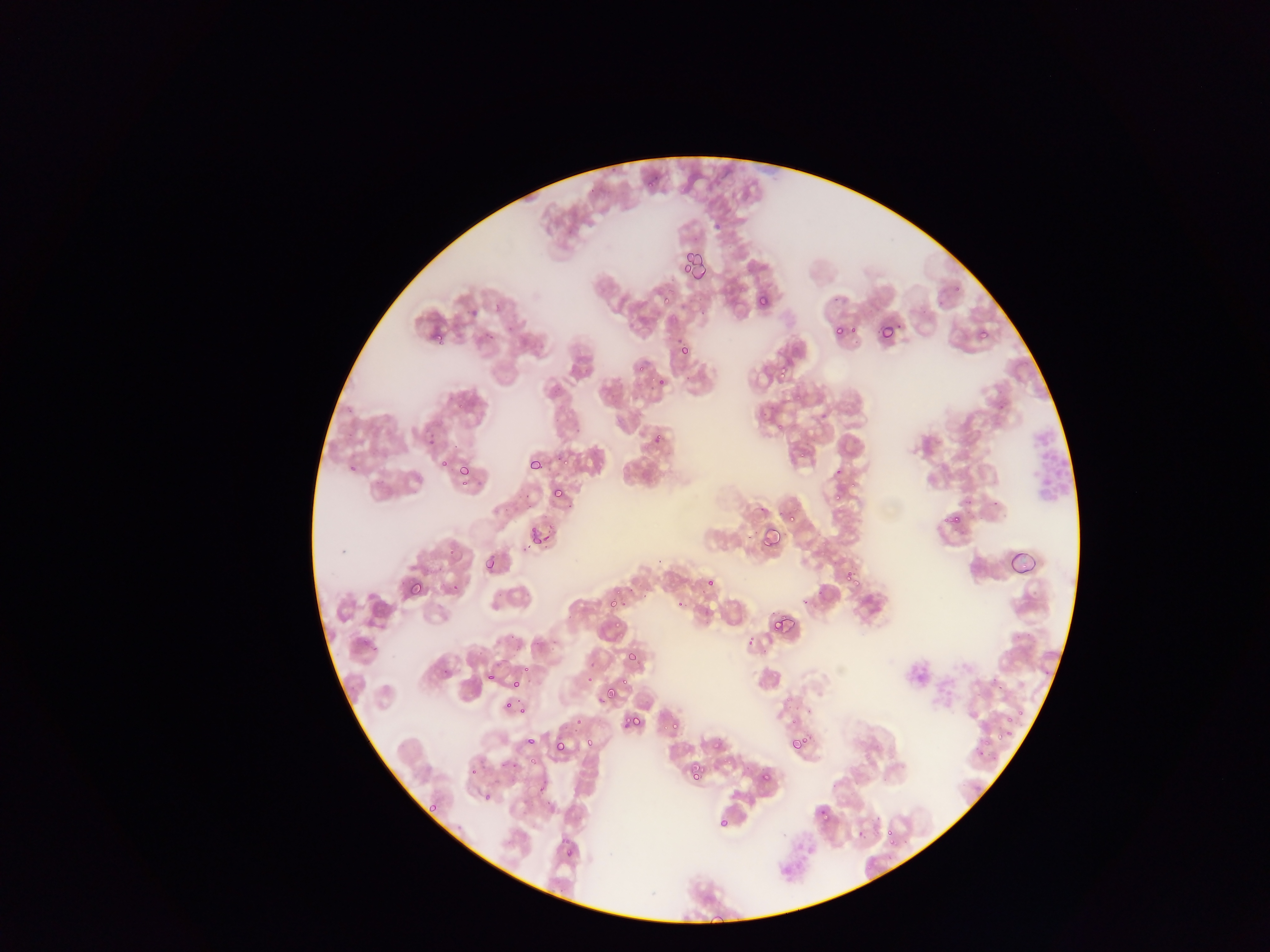
Approximate bounding boxes as [left, top, right, bottom] in pixels.
Summary:
  - Leukocyte locations: [1030, 420, 1073, 507]
  - Plasmodium parasite locations: [646, 181, 654, 189], [687, 242, 711, 276], [679, 258, 693, 275], [658, 289, 675, 310], [494, 295, 509, 315], [758, 295, 770, 308], [462, 301, 482, 318], [508, 318, 519, 338], [833, 324, 844, 336], [848, 324, 858, 336], [877, 324, 893, 342], [482, 326, 498, 341], [977, 329, 988, 340], [431, 330, 442, 341], [679, 343, 690, 355], [776, 361, 791, 375], [635, 362, 646, 372], [654, 374, 671, 391], [775, 422, 788, 436], [425, 429, 441, 452], [653, 435, 666, 440], [796, 450, 807, 463], [440, 459, 450, 469], [531, 459, 544, 470], [829, 461, 847, 477], [349, 464, 356, 472], [458, 465, 471, 478], [849, 476, 858, 489], [457, 479, 470, 489], [553, 487, 564, 499], [832, 490, 843, 501], [750, 502, 773, 517], [782, 510, 794, 523], [946, 512, 962, 527], [530, 521, 540, 541], [759, 526, 779, 549], [539, 534, 551, 545], [1006, 552, 1040, 582], [485, 558, 495, 570], [845, 570, 860, 587], [407, 576, 427, 594], [706, 578, 715, 586], [448, 582, 459, 594], [799, 584, 826, 608], [609, 596, 620, 610], [675, 599, 683, 608], [611, 615, 624, 632], [769, 618, 786, 633], [745, 631, 758, 652], [627, 648, 636, 665], [523, 664, 533, 673], [585, 668, 598, 682], [486, 672, 494, 682], [617, 675, 630, 688], [510, 678, 521, 688], [604, 683, 619, 704], [503, 699, 518, 712], [516, 703, 527, 719], [1018, 705, 1026, 717], [571, 713, 583, 728], [1003, 714, 1012, 727], [629, 715, 643, 728], [671, 720, 681, 732], [1007, 728, 1016, 737], [995, 734, 1002, 742], [789, 736, 806, 751], [583, 737, 593, 747], [982, 737, 991, 750], [525, 738, 535, 746], [712, 739, 725, 751], [553, 741, 566, 754], [525, 757, 540, 770], [690, 764, 704, 779], [469, 766, 478, 777], [761, 772, 771, 782], [763, 776, 773, 783], [482, 792, 492, 803], [429, 803, 439, 811], [818, 806, 828, 816], [717, 817, 729, 827], [884, 819, 898, 834], [855, 831, 867, 841], [890, 835, 899, 847], [564, 848, 574, 858]
  - Preparation: thin blood film
  - Capture: mobile-phone photograph through a microscope
  - Image size: 1270×952 pixels
  - Country: Ghana
  - Field of view: single